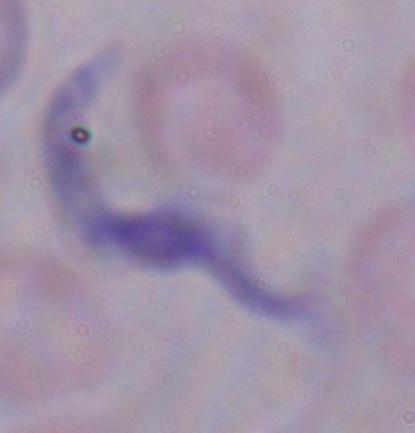
Photomicrograph. A trypanosome is shown. 1000x magnification.